Classify this cell by malaria status.
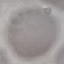

Uninfected.

Summary:
  - Preparation: thin blood film
  - Image type: cell patch, automatically extracted from a larger field of view and resized to 64 × 64 pixels
  - Capture: smartphone through the microscope eyepiece
  - Stain: Giemsa